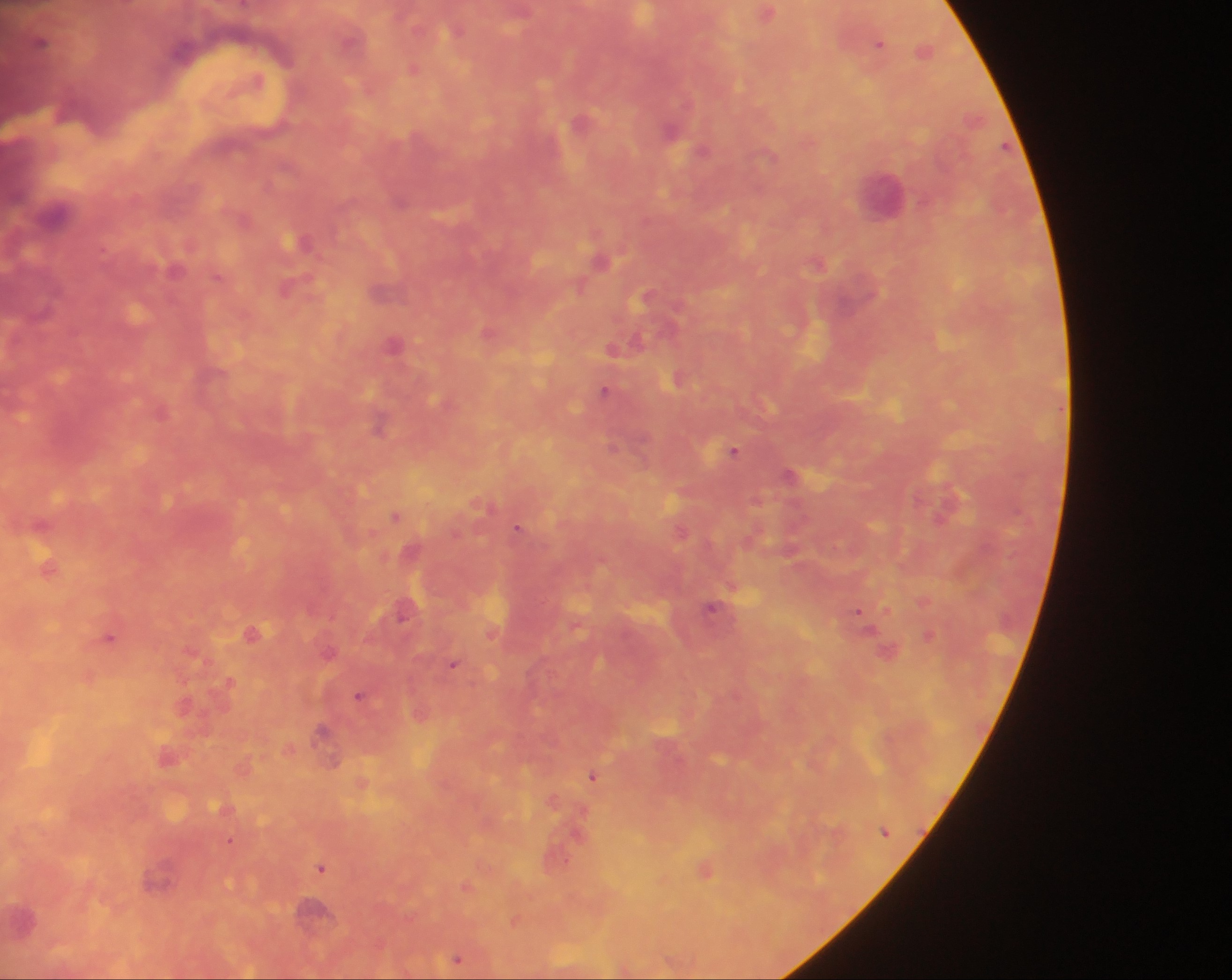

Plasmodium parasite locations = approximate centers as (x, y) in pixels: (766, 13), (41, 40), (878, 42), (925, 50), (414, 68), (671, 133), (401, 199), (55, 211), (302, 240), (819, 262), (288, 287), (647, 295), (395, 343), (613, 348), (675, 378), (604, 390), (380, 424), (613, 445), (735, 450), (789, 473), (756, 500), (394, 515), (518, 526), (680, 531), (47, 566), (712, 607), (404, 609), (858, 612), (254, 631), (929, 633), (108, 636), (329, 650), (888, 651), (453, 663), (229, 681), (360, 695), (322, 730), (593, 775), (230, 839), (321, 867), (705, 870), (158, 876), (456, 957)
field of view = single
capture = mobile-phone photograph through a microscope
image size = 1232×980 pixels
preparation = thick blood film
country = Ghana
leukocyte locations = approximate centers as (x, y) in pixels: (884, 191)